Describe the morphology of the erythrocytes.
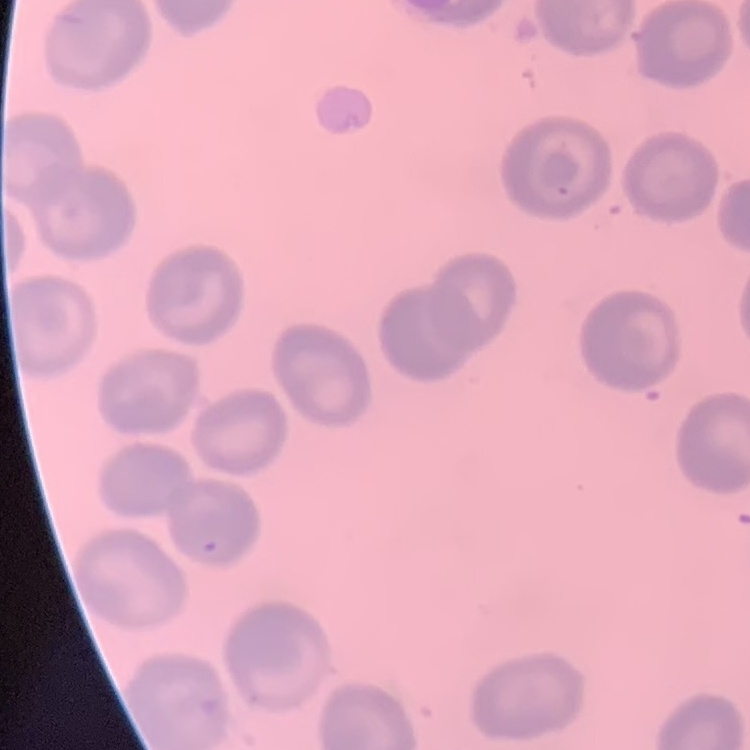
No rouleaux formation.

Field's or Giemsa stain. Thin blood film. Square crop of a larger photomicrograph.